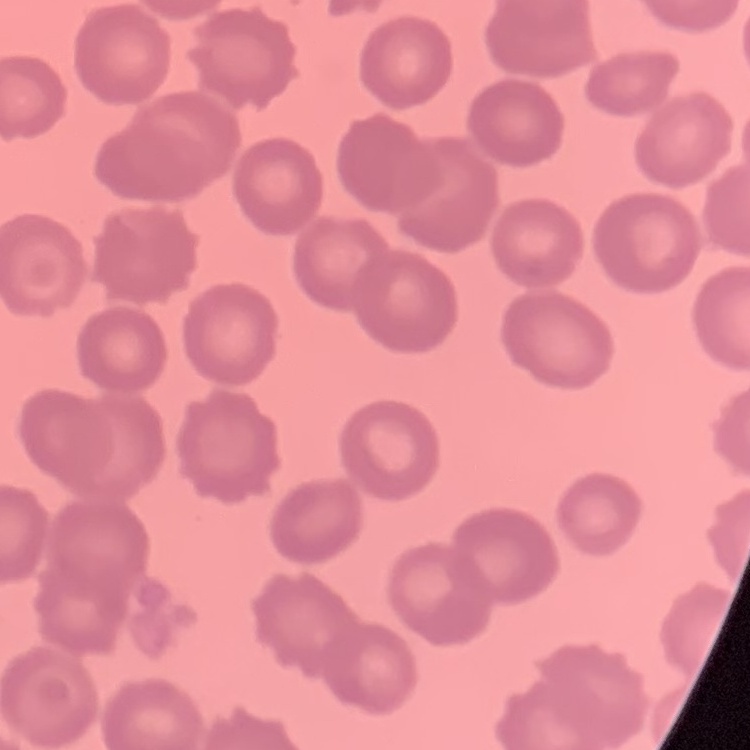 The erythrocytes exhibit no rouleaux formation. One tile cut from a larger photomicrograph. Thin peripheral smear. Stained with either Field's or Giemsa.